Mark where leukocytes are.
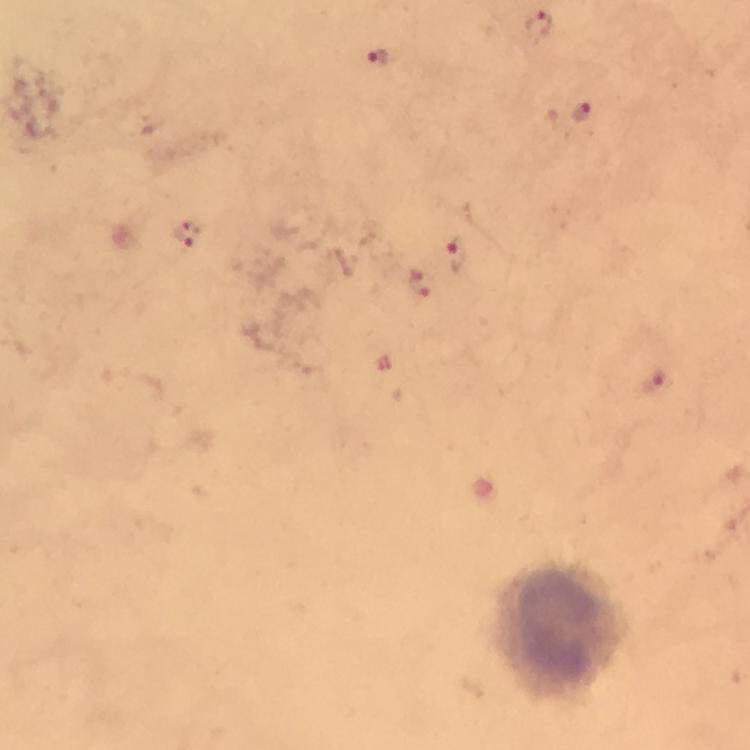

Approximate object centers, in pixels from the top-left corner.
Leukocytes: (x=560, y=626).

Summary:
  - Malaria parasite locations: (x=538, y=26), (x=377, y=58), (x=582, y=113), (x=188, y=235), (x=456, y=254), (x=419, y=285), (x=656, y=383)
  - Stain: Giemsa
  - Capture: smartphone mounted on the microscope
  - Cropped from: a single field of view
  - Magnification: 100x
  - Immersion oil: used
  - Image size: 750×750 pixels
  - Preparation: thick smear
  - Context: from a malaria diagnostic workup